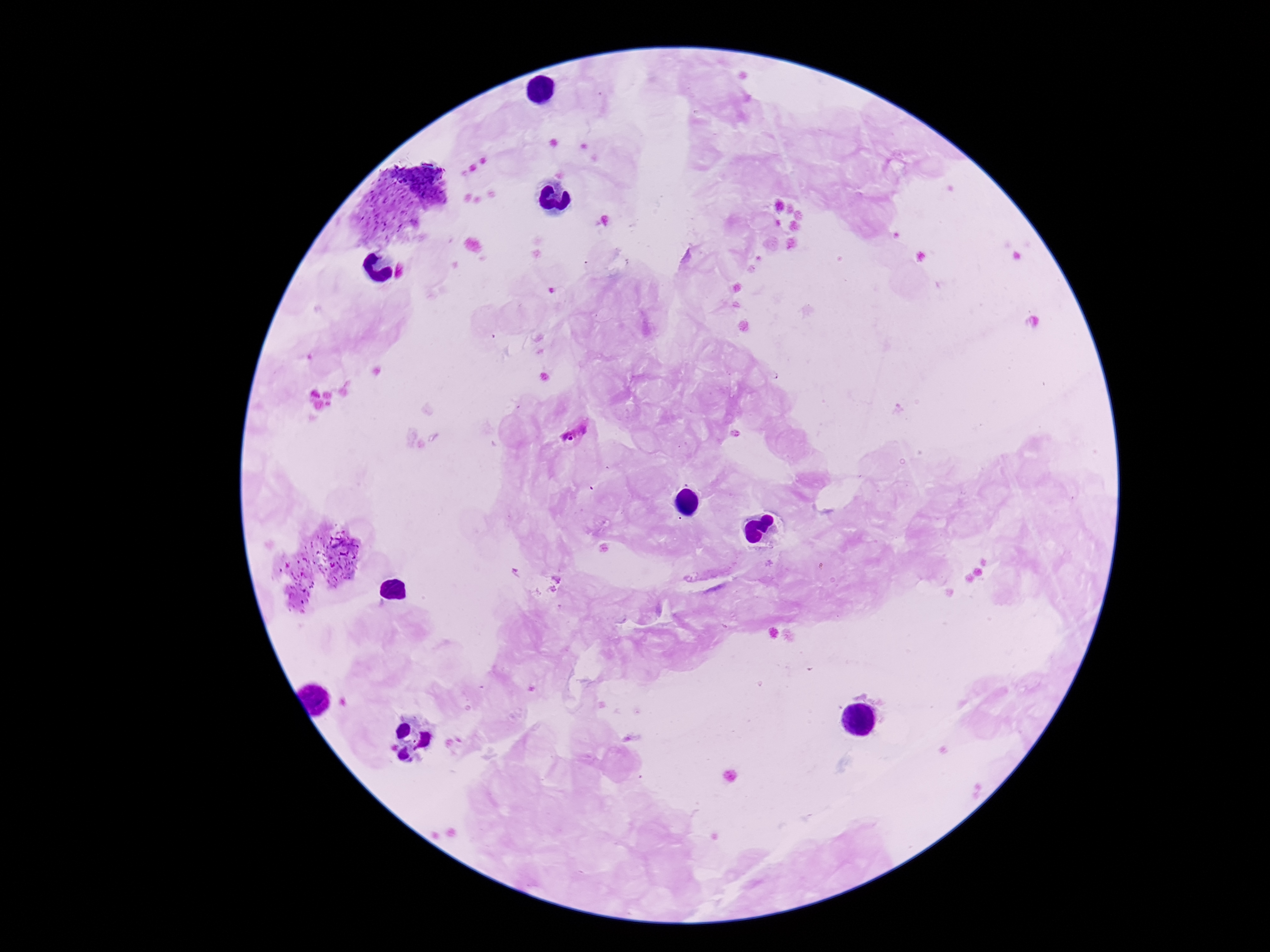
Approximate object centers, in pixels from the top-left corner. Plasmodium parasite locations: (x=572, y=432). Smartphone photograph taken through the microscope eyepiece. Giemsa-stained preparation. Thick blood film. 100x magnification. One field from this slide. Patient malaria status: positive. Image is 1270×952 pixels.